Describe the morphology of the red blood cells.
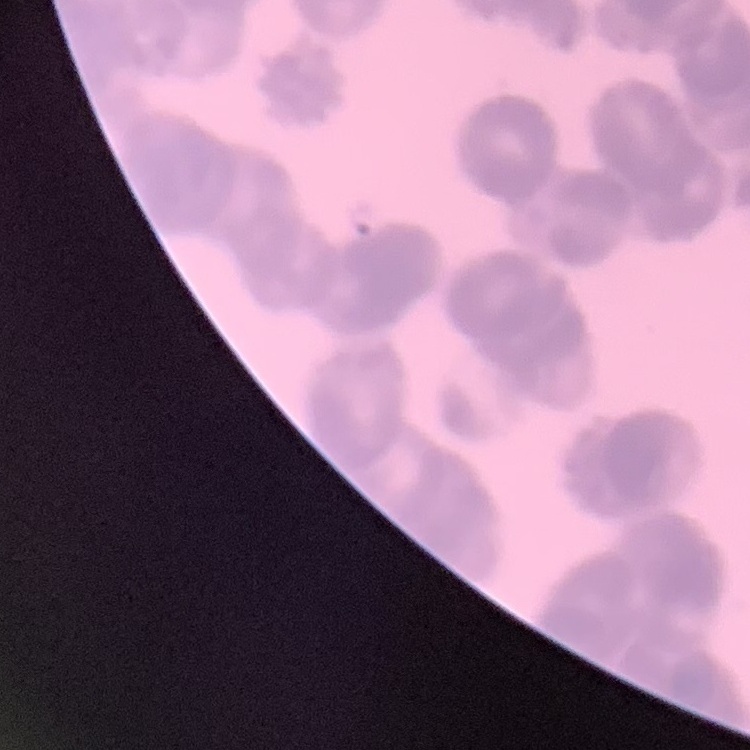
They show rouleaux formation.

Summary:
  - Preparation: thin blood film
  - Stain: Field's or Giemsa
  - Image type: one tile cut from a larger photomicrograph